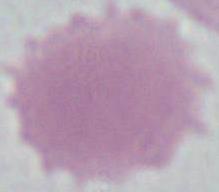 Micrograph. A red blood cell is shown. 1000x magnification.